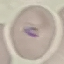

Summary:
  - Malaria status: parasitized
  - Stain: Giemsa
  - Image type: automatically extracted cell patch, resized to 64 × 64 pixels
  - Preparation: thin blood smear
  - Capture: smartphone through the microscope eyepiece